Point out each Plasmodium parasite.
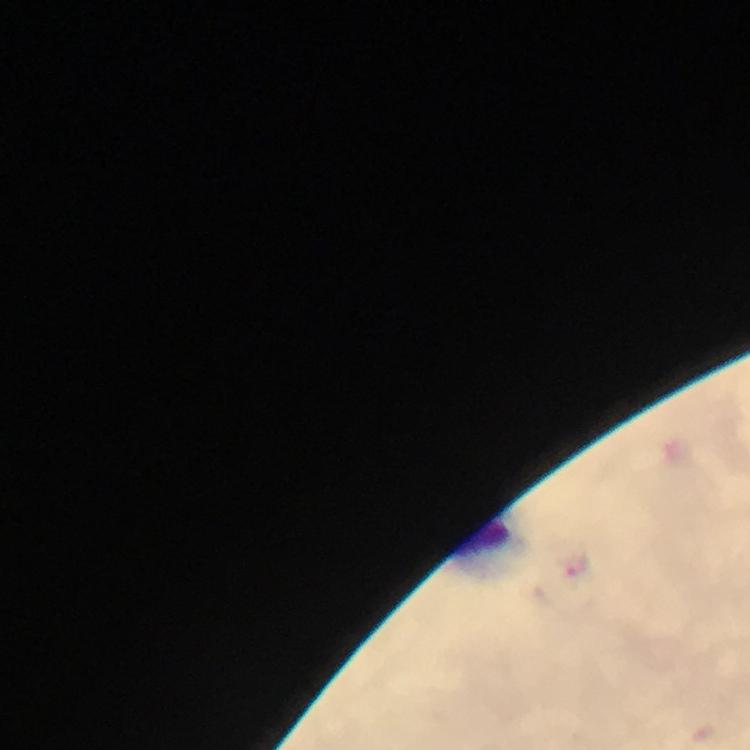

No Plasmodium parasites detected.

Approximate centers as [x, y] in pixels.
Summary:
  - Leukocyte locations: [487, 545]
  - Context: from a malaria diagnostic workup
  - Image size: 750×750 pixels
  - Cropped from: one field of view
  - Immersion oil: applied
  - Magnification: 100x
  - Capture: smartphone photograph through a microscope
  - Stain: Giemsa
  - Preparation: thick blood film